Point out every malaria parasite and every leukocyte.
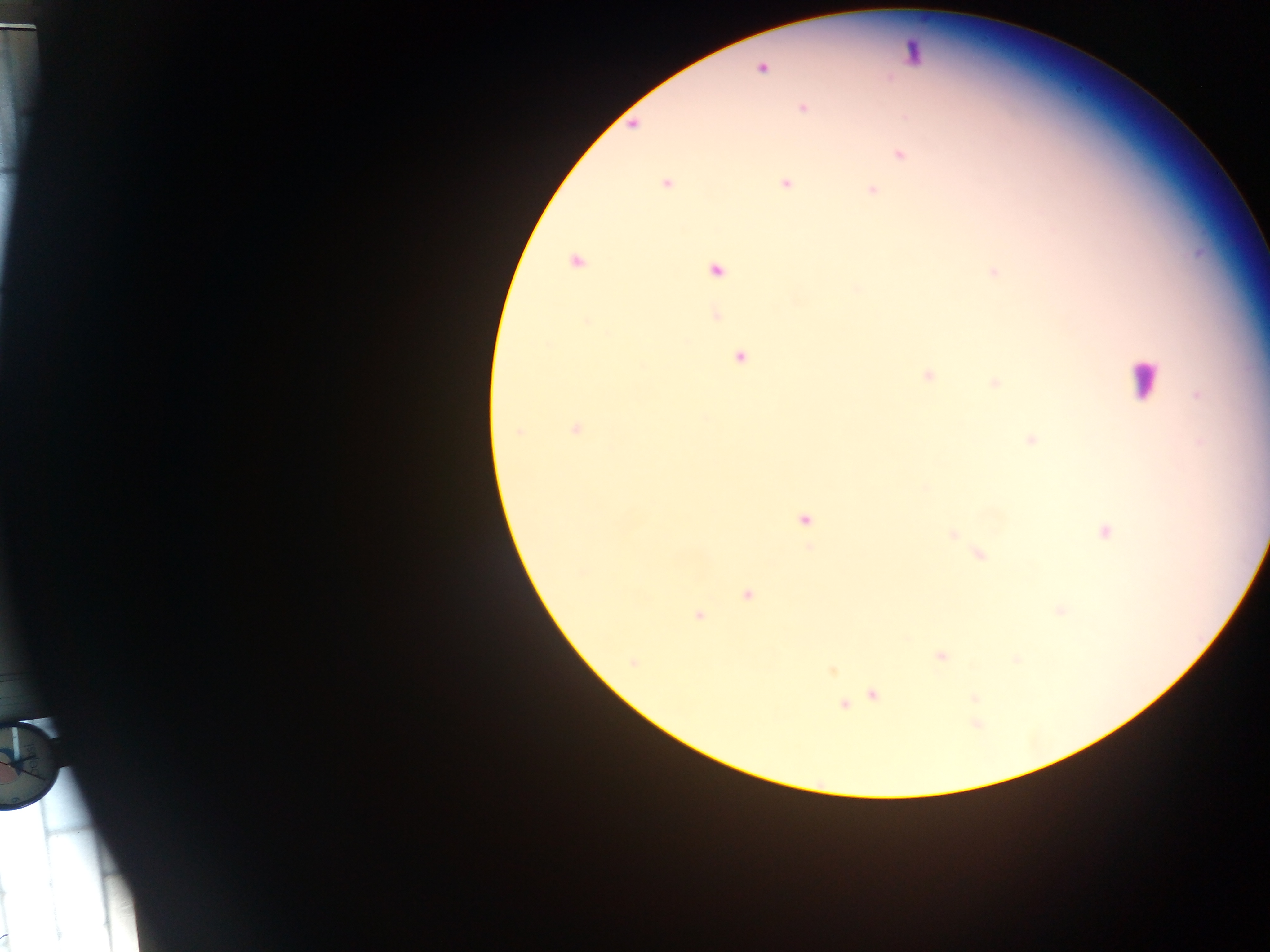
Approximate centers as {x, y} in pixels.
Malaria parasites: {761, 68}, {802, 107}, {631, 124}, {898, 153}, {664, 183}, {785, 183}, {870, 189}, {573, 264}, {716, 271}, {993, 272}, {857, 290}, {713, 315}, {588, 321}, {548, 345}, {739, 357}, {927, 374}, {993, 382}, {576, 428}, {518, 432}, {1029, 439}, {925, 488}, {805, 519}, {1104, 530}, {952, 534}, {809, 548}, {978, 554}, {747, 594}, {1060, 610}, {698, 613}, {942, 656}, {1017, 659}, {832, 672}, {874, 694}, {976, 698}, {845, 706}, {976, 725}, {8, 935}.
Leukocytes: {1143, 381}.

Sample from Ghana. Photographed through a microscope with a mobile-phone camera. Image is 1270×952 pixels. Thick blood smear. One field of view.